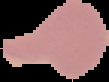
{
  "result": "no Plasmodium parasites detected",
  "preparation": "thin blood film",
  "image_type": "segmented cell region with the area outside set to black",
  "image_size": "109×82 pixels"
}